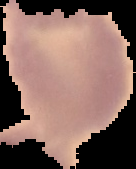 The area outside the segmented cell region is set to black. Result: no malaria parasites seen. Image is 136×169 pixels. From a thin blood smear.